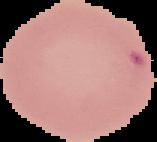

From a thin blood film. Image is 157×142 pixels. The area outside the segmented cell region is set to black. Result: no Plasmodium parasites detected.